Locate platelets.
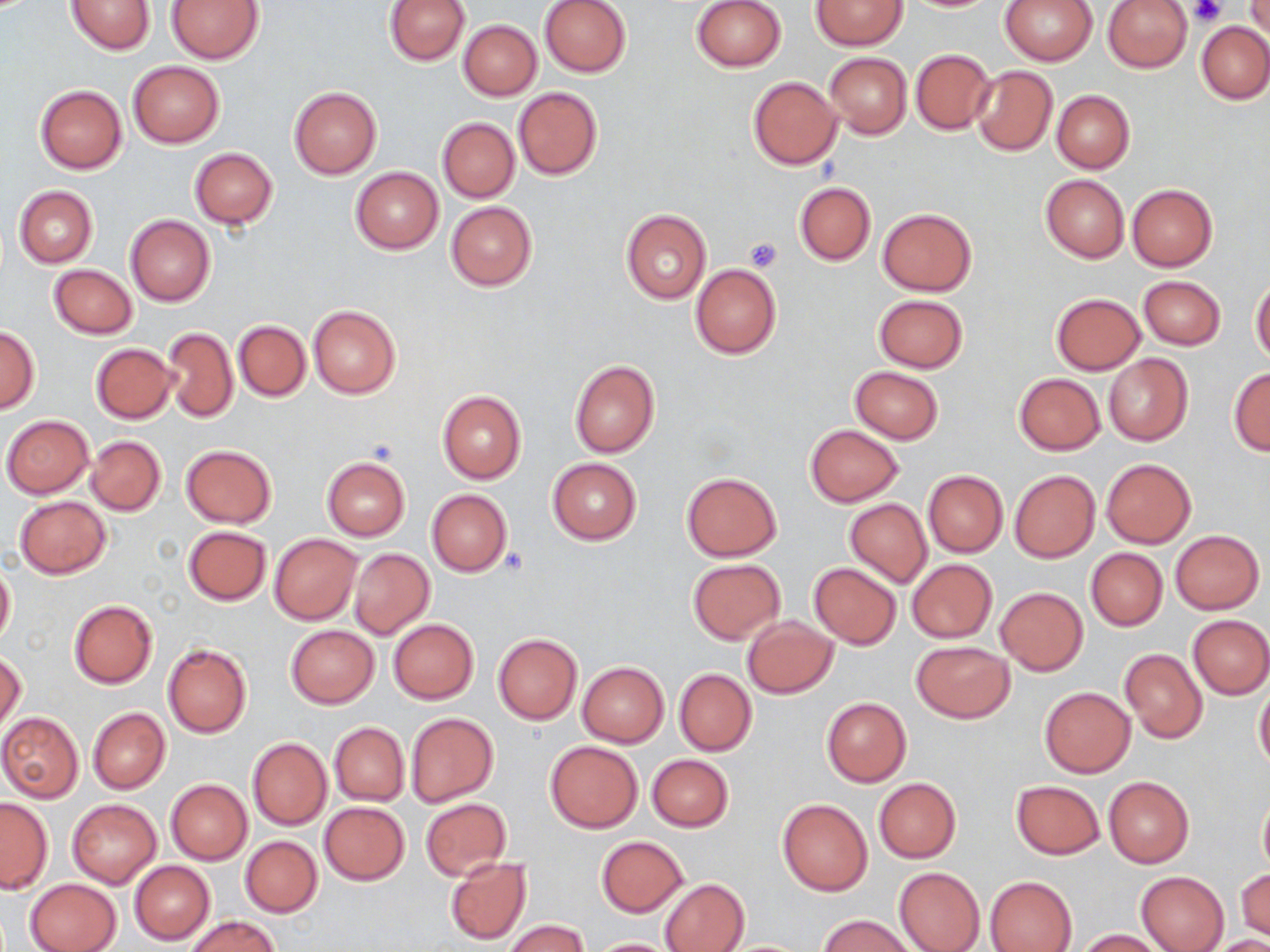

Approximate bounding boxes as [x1, y1, x2, y2] in pixels.
Platelets: [1190, 0, 1227, 27], [744, 236, 783, 273].

Uninfected red blood cell locations: [385, 0, 471, 66], [539, 0, 631, 78], [690, 0, 786, 73], [811, 0, 908, 50], [999, 0, 1097, 65], [1103, 0, 1191, 73], [65, 1, 155, 54], [166, 1, 262, 63], [1245, 1, 1270, 39], [458, 20, 541, 100], [1197, 21, 1270, 103], [910, 49, 996, 136], [823, 52, 912, 137], [127, 61, 225, 148], [971, 66, 1057, 156], [748, 77, 842, 170], [35, 84, 127, 172], [289, 86, 382, 179], [513, 87, 602, 180], [1051, 90, 1134, 173], [437, 117, 519, 202], [189, 148, 277, 228], [349, 167, 443, 254], [1040, 174, 1129, 262], [794, 181, 875, 265], [1127, 183, 1218, 271], [13, 185, 97, 267], [445, 201, 537, 291], [877, 208, 976, 295], [621, 210, 711, 303], [125, 214, 215, 306], [49, 264, 137, 339], [690, 264, 781, 359], [1138, 275, 1226, 350], [1251, 280, 1270, 366], [1051, 293, 1145, 374], [873, 294, 967, 372], [308, 304, 400, 398], [233, 320, 310, 402], [0, 325, 39, 413], [160, 325, 237, 423], [91, 343, 175, 422], [1103, 354, 1192, 446], [569, 360, 660, 458], [849, 365, 944, 444], [1228, 368, 1270, 455], [1013, 373, 1105, 454], [436, 390, 526, 484], [2, 415, 93, 498], [803, 424, 905, 507], [84, 436, 166, 515], [180, 444, 276, 528], [546, 457, 642, 545], [321, 458, 410, 540], [1101, 458, 1196, 548], [1008, 468, 1100, 563], [923, 470, 1008, 557], [681, 472, 782, 562], [426, 489, 514, 576], [14, 496, 110, 579], [844, 497, 931, 588], [183, 526, 271, 605], [1169, 530, 1264, 614], [269, 534, 361, 625], [1085, 547, 1167, 631], [349, 548, 434, 639], [907, 559, 997, 642], [0, 560, 15, 647], [687, 560, 784, 644], [809, 563, 901, 648], [995, 588, 1088, 675], [68, 600, 158, 689], [1187, 614, 1269, 699], [743, 618, 837, 699], [388, 619, 479, 704], [286, 625, 379, 707], [493, 633, 582, 724], [910, 641, 1015, 722], [163, 644, 252, 739], [1120, 649, 1207, 742], [0, 652, 26, 737], [577, 661, 668, 746], [674, 668, 756, 755], [1253, 681, 1270, 772], [1038, 687, 1136, 778], [822, 697, 911, 786], [87, 707, 170, 793], [405, 712, 498, 806], [0, 713, 83, 802], [329, 722, 408, 805], [247, 737, 331, 830], [544, 740, 642, 833], [645, 753, 733, 832], [1103, 776, 1193, 867], [873, 778, 961, 863], [166, 779, 252, 864], [1010, 780, 1103, 859], [1257, 791, 1270, 877], [0, 797, 51, 893], [421, 798, 511, 880], [777, 798, 873, 895], [67, 799, 160, 887], [319, 802, 409, 885], [241, 837, 322, 916], [596, 837, 687, 916], [445, 857, 533, 945], [129, 861, 215, 944], [894, 866, 986, 952], [1235, 867, 1270, 941], [1136, 871, 1229, 952], [985, 876, 1077, 952], [25, 877, 121, 952], [660, 878, 747, 952], [819, 915, 914, 952], [184, 916, 280, 952], [502, 919, 591, 952], [1073, 929, 1165, 951], [1204, 935, 1270, 951], [589, 937, 680, 951]. Slide-level diagnosis: no evidence of blood parasites. 1000x magnification. Light microscopy. Image is 1270×952 pixels. Single field of view. Thin blood film. May-Grünwald-Giemsa-stained preparation.